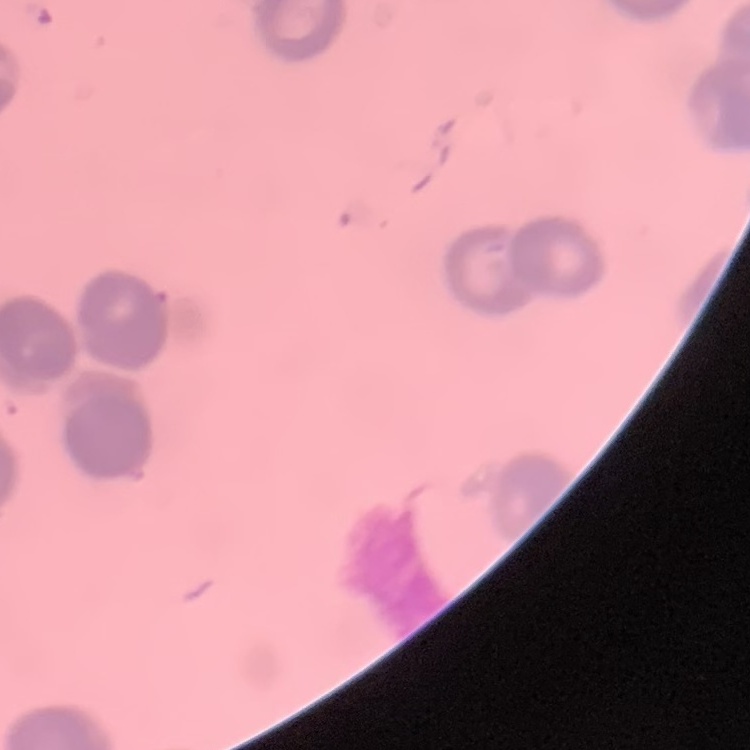
Summary:
  - Erythrocyte morphology: rouleaux formation
  - Stain: Field's or Giemsa
  - Image type: square crop of a larger photomicrograph
  - Preparation: thin blood film